Locate every malaria parasite.
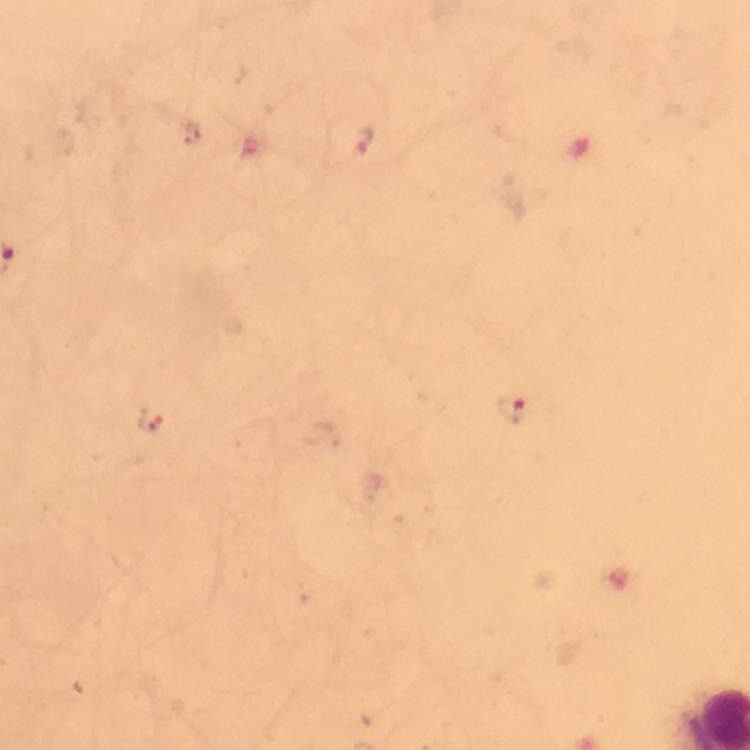

Approximate centers as [x, y] in pixels.
Malaria parasites: [363, 141], [511, 410], [152, 421].

Summary:
  - Preparation: thick blood film
  - Cropped from: one field of view
  - Image size: 750×750 pixels
  - Context: from a malaria diagnostic workup
  - Immersion oil: used
  - Capture: smartphone photograph through a microscope
  - Stain: Giemsa
  - Magnification: 100x